Report the malaria status of this cell.
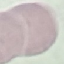
It is uninfected.

image type = cell patch, automatically extracted from a larger field of view and resized to 64 × 64 pixels
capture = smartphone through the microscope eyepiece
preparation = thin smear
stain = Giemsa